Give the position of every Plasmodium parasite visible.
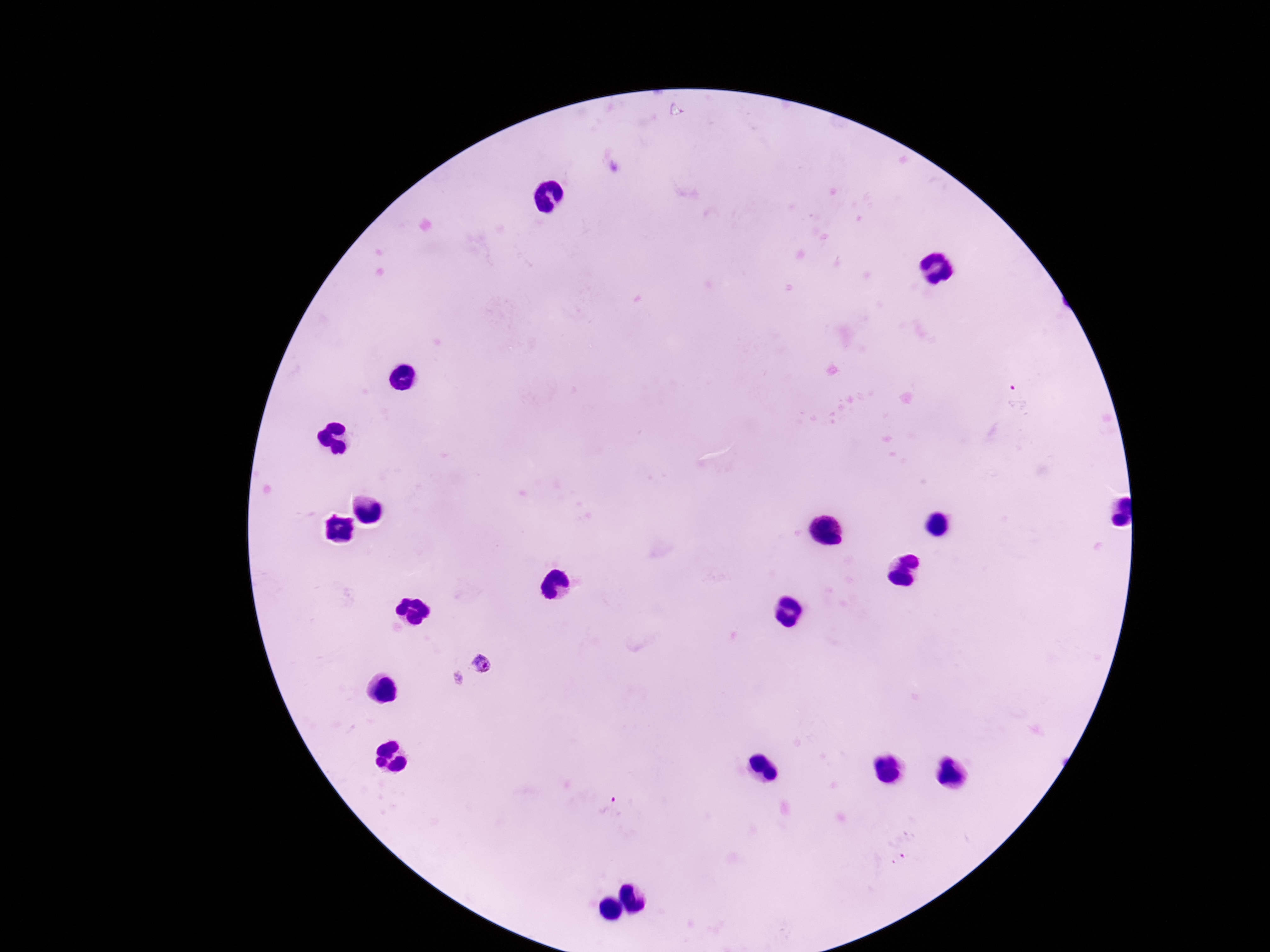

Approximate centers as {x, y} in pixels.
Plasmodium parasites: {484, 666}, {607, 807}.

Thick blood smear. Single field of view. Patient malaria status: positive. 100x magnification. Giemsa stain. Image is 1270×952 pixels. Smartphone photograph taken through the microscope eyepiece.